Report the malaria status of this cell.
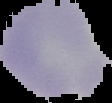

Uninfected.

image size = 112×103 pixels
preparation = thin blood film
image type = segmented cell region with the area outside set to black